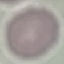
Summary:
  - Malaria status: uninfected
  - Preparation: thin blood film
  - Stain: Giemsa
  - Capture: smartphone through the microscope eyepiece
  - Image type: automatically extracted cell patch, resized to 64 × 64 pixels